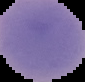
From a thin blood smear. Cell region segmented out of the field of view; the surrounding area is masked to black. Malaria status: uninfected. Image is 85×82 pixels.